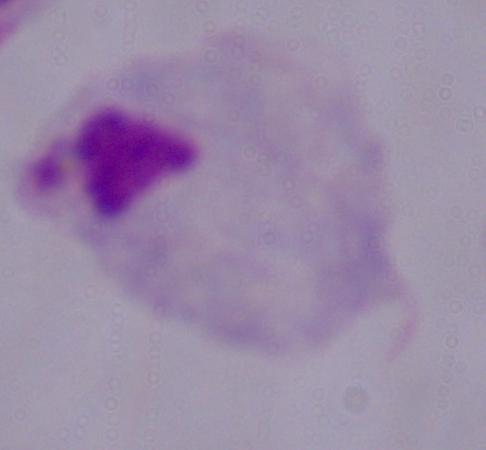
Summary:
  - Magnification: 1000x
  - Modality: photomicrograph
  - Identification: trichomonad